Give the position of every Plasmodium parasite visible.
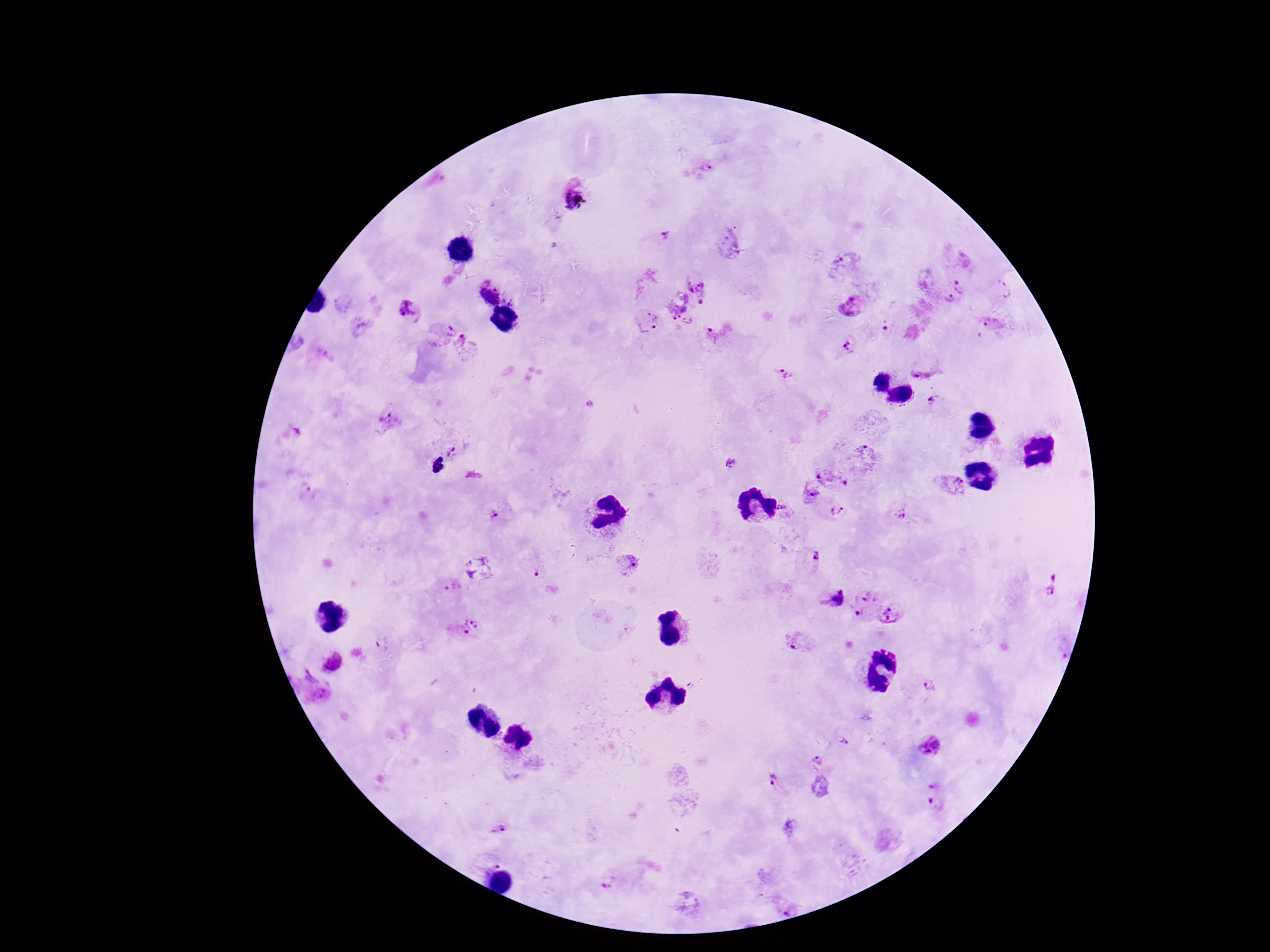
Approximate centers as [x, y] in pixels.
Plasmodium parasites: [702, 168], [575, 197], [661, 237], [961, 284], [702, 287], [1002, 288], [489, 295], [947, 299], [853, 304], [408, 309], [648, 322], [684, 324], [993, 324], [441, 331], [716, 332], [466, 347], [848, 348], [785, 373], [936, 405], [390, 422], [451, 451], [867, 455], [733, 463], [832, 479], [952, 484], [811, 494], [781, 507], [838, 512], [495, 514], [899, 515], [811, 558], [628, 563], [478, 567], [532, 572], [1056, 584], [453, 587], [832, 597], [874, 608], [466, 626], [798, 641], [332, 662], [929, 685], [927, 746], [818, 760], [774, 783], [937, 794], [496, 826], [491, 862], [606, 883], [789, 906].

Summary:
  - Patient malaria status: infected
  - Field of view: one from this slide
  - Capture: smartphone camera through the microscope eyepiece
  - Image size: 1270×952 pixels
  - Magnification: 100x
  - Preparation: thick blood film
  - Stain: Giemsa